Give the position of every malaria parasite.
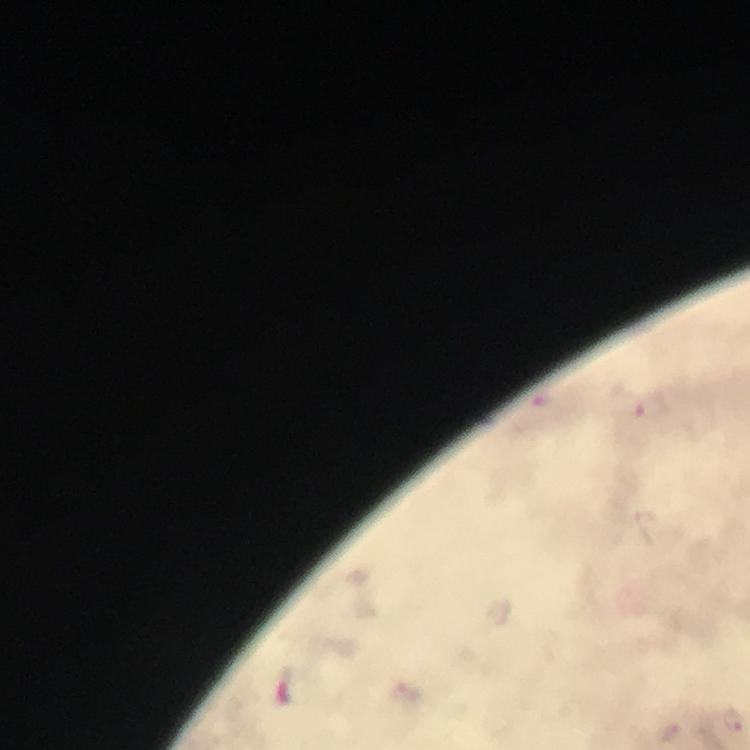
Approximate centers as {x, y} in pixels.
Malaria parasites: {654, 409}, {733, 718}.

{
  "context": "from a diagnostic examination for malaria",
  "image_size": "750×750 pixels",
  "stain": "Giemsa",
  "capture": "smartphone photograph through a microscope",
  "cropped_from": "one field of view",
  "immersion_oil": "used",
  "preparation": "thick smear",
  "magnification": "100x"
}